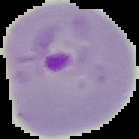

Cell region segmented out of the field of view; the surrounding area is masked to black. From a thin blood film. Malaria status: parasitized. Image is 139×139 pixels.